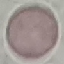 Result: no malaria parasites seen. Thin blood smear. Acquired by smartphone through the microscope eyepiece. Giemsa stain. Automatically extracted cell patch, resized to 64 × 64 pixels.